Locate every blood parasite and identify its species.
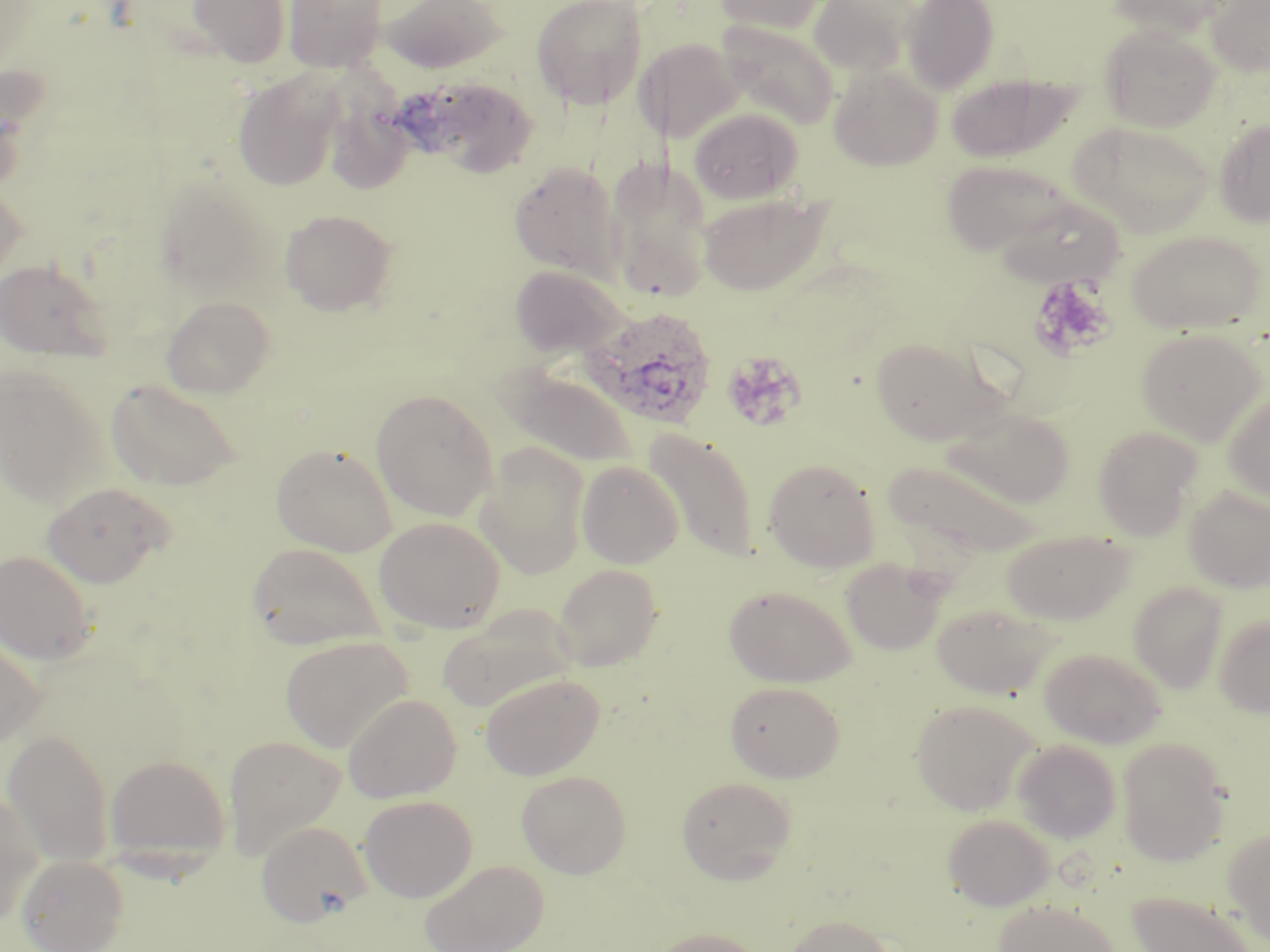

Approximate bounding boxes as (x1, y1, x2, y2) in pixels.
Plasmodium ovale-infected red blood cells: (580, 304, 718, 430).
No Plasmodium falciparum, Plasmodium malariae, Plasmodium vivax, Babesia divergens, or Trypanosoma brucei observed.

Uninfected red blood cell locations: (186, 0, 293, 68), (284, 0, 388, 74), (379, 0, 508, 74), (532, 0, 648, 110), (712, 0, 831, 34), (809, 0, 917, 78), (902, 0, 999, 93), (1110, 0, 1233, 37), (1205, 0, 1270, 77), (718, 20, 838, 129), (1101, 25, 1220, 132), (637, 38, 744, 144), (828, 64, 943, 171), (232, 71, 343, 190), (945, 73, 1077, 163), (407, 76, 541, 179), (325, 93, 417, 195), (689, 107, 804, 204), (1214, 119, 1270, 227), (1069, 121, 1213, 237), (604, 157, 714, 302), (942, 158, 1079, 257), (509, 161, 623, 279), (154, 176, 277, 299), (0, 178, 27, 286), (698, 191, 830, 296), (992, 195, 1126, 287), (280, 209, 398, 316), (1124, 228, 1266, 335), (0, 258, 112, 362), (509, 264, 627, 359), (162, 295, 276, 398), (1135, 327, 1266, 443), (870, 337, 1001, 445), (0, 366, 105, 504), (500, 369, 640, 469), (105, 378, 242, 491), (1222, 387, 1270, 504), (371, 388, 497, 521), (942, 406, 1076, 507), (1093, 426, 1202, 539), (644, 428, 759, 561), (475, 442, 591, 579), (271, 443, 397, 556), (763, 458, 880, 571), (883, 459, 1039, 559), (577, 460, 684, 568), (42, 481, 173, 588), (1184, 486, 1270, 593), (374, 516, 506, 634), (1001, 529, 1135, 625), (246, 542, 386, 653), (0, 549, 97, 664), (841, 558, 946, 655), (553, 564, 663, 670), (1129, 582, 1227, 693), (723, 583, 856, 686), (932, 602, 1056, 699), (438, 604, 577, 712), (1214, 614, 1270, 717), (0, 634, 46, 751), (281, 636, 413, 752), (1039, 647, 1167, 748), (480, 673, 605, 780), (725, 681, 845, 782), (343, 693, 461, 803), (911, 699, 1040, 815), (3, 729, 114, 866), (223, 734, 347, 860), (1116, 737, 1232, 866), (1012, 739, 1121, 843), (104, 754, 230, 865), (517, 769, 632, 878), (676, 776, 797, 883), (0, 786, 44, 927), (359, 795, 477, 901), (942, 813, 1055, 911), (257, 820, 371, 927), (1223, 828, 1270, 946), (17, 852, 128, 951), (419, 859, 548, 952), (1126, 891, 1262, 952), (993, 899, 1122, 952), (783, 914, 900, 952), (649, 927, 767, 952). Platelet locations: (1029, 275, 1115, 360), (721, 351, 807, 432). Slide-level diagnosis: Plasmodium ovale. Captured at 1000x magnification. One field of a larger specimen. Optical microscopy. May-Grünwald-Giemsa-stained preparation. Thin blood film. Image is 1270×952 pixels.